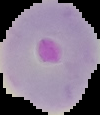
Image is 100×115 pixels. Malaria status: parasitized. Cell region segmented out of the field of view; the surrounding area is masked to black. From a thin blood smear.